State which parasite is depicted.
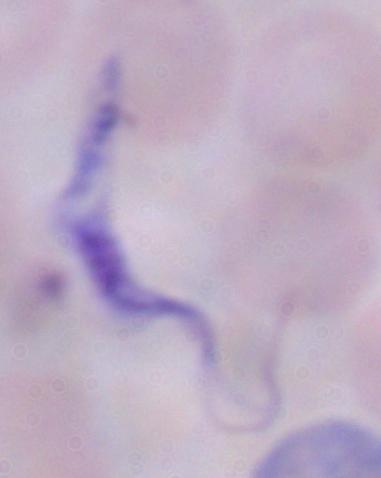

A trypanosome.

Summary:
  - Modality: micrograph
  - Magnification: 1000x